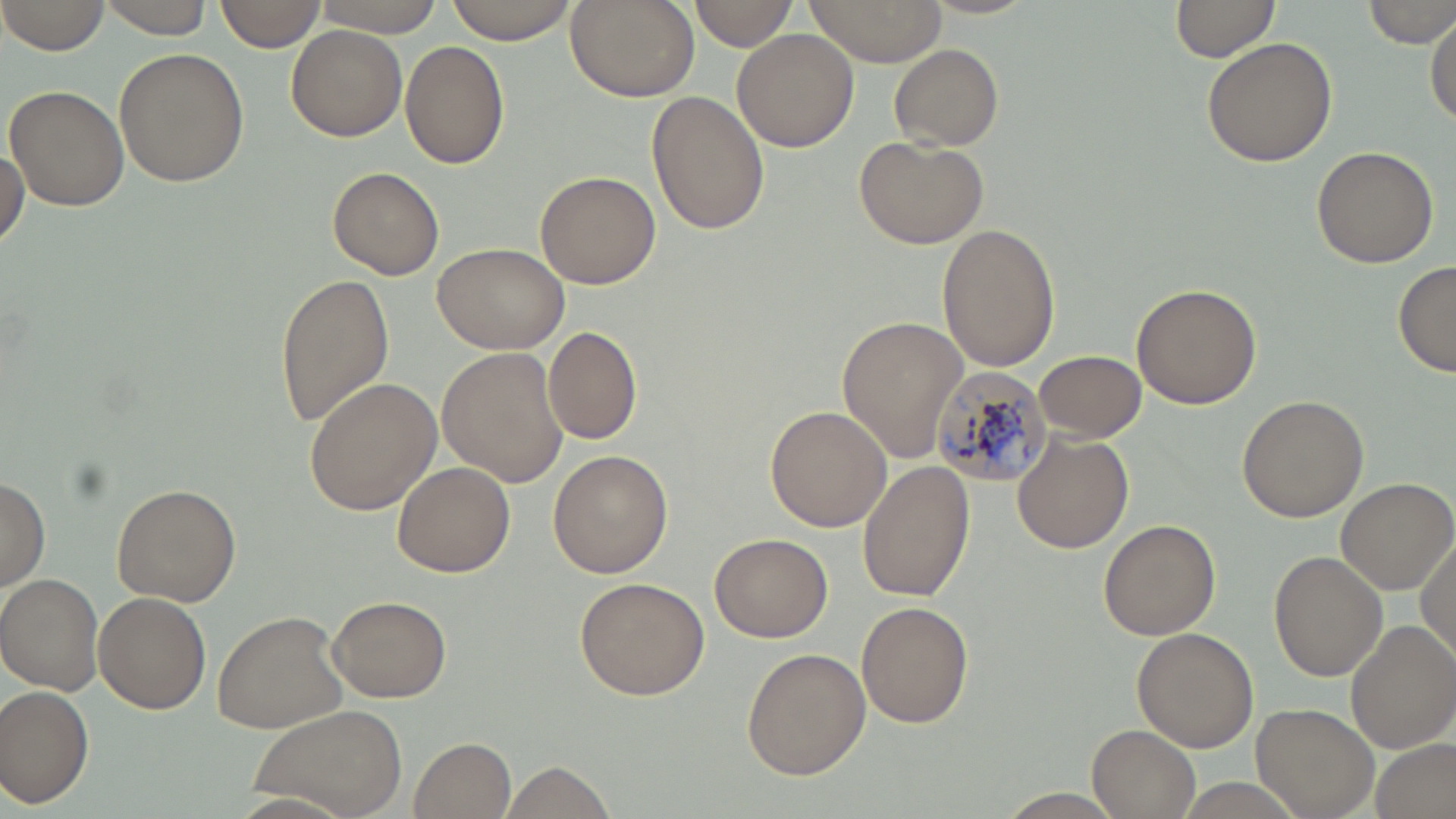
slide-level diagnosis = Plasmodium malariae
stain = May-Grünwald-Giemsa
modality = optical microscopy
Plasmodium malariae-infected red blood cell locations = approximate bounding boxes as [x1, y1, x2, y2] in pixels: [928, 366, 1053, 486]
image size = 1456×819 pixels
magnification = 1000x
preparation = thin blood smear
field of view = one of a larger specimen
uninfected red blood cell locations = approximate bounding boxes as [x1, y1, x2, y2] in pixels: [1, 0, 110, 55], [96, 0, 218, 36], [215, 0, 324, 53], [442, 0, 583, 44], [564, 0, 699, 103], [801, 0, 951, 66], [305, 1, 448, 36], [688, 1, 799, 50], [1170, 1, 1281, 65], [1365, 1, 1456, 48], [1427, 14, 1455, 126], [286, 25, 406, 141], [732, 29, 858, 153], [1201, 36, 1338, 168], [401, 40, 510, 170], [890, 44, 1003, 149], [113, 47, 251, 187], [4, 84, 129, 212], [646, 92, 770, 236], [852, 135, 988, 249], [1, 142, 28, 249], [1311, 143, 1441, 268], [329, 167, 445, 280], [535, 170, 660, 290], [937, 224, 1061, 371], [430, 241, 570, 353], [1392, 261, 1455, 378], [276, 269, 395, 427], [1132, 283, 1261, 408], [839, 315, 971, 464], [542, 325, 642, 445], [437, 348, 568, 487], [1035, 349, 1144, 442], [304, 377, 441, 515], [1237, 394, 1368, 522], [765, 404, 892, 533], [1013, 432, 1131, 553], [548, 448, 674, 578], [858, 459, 975, 601], [392, 461, 515, 578], [0, 475, 49, 593], [1335, 475, 1455, 595], [112, 482, 241, 607], [1099, 519, 1220, 640], [710, 532, 834, 641], [1415, 533, 1455, 661], [1269, 549, 1388, 683], [1, 575, 104, 694], [574, 577, 710, 701], [95, 592, 211, 714], [328, 596, 451, 702], [856, 602, 973, 728], [211, 609, 350, 734], [1345, 619, 1456, 754], [1132, 628, 1258, 752], [742, 646, 871, 779], [0, 685, 95, 808], [1253, 701, 1381, 819], [246, 704, 409, 819], [1086, 725, 1201, 818], [412, 735, 517, 816], [1374, 737, 1453, 819], [504, 762, 617, 817], [985, 789, 1134, 819]